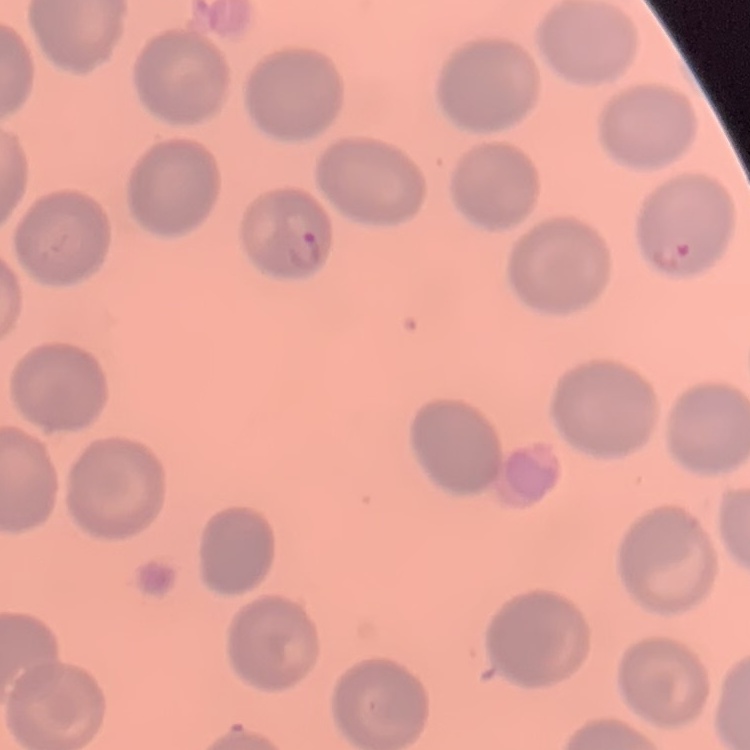
red_blood_cell_morphology: no rouleaux formation
preparation: thin blood smear
image_type: one tile cut from a larger photomicrograph
stain: Field's or Giemsa